Report the malaria status.
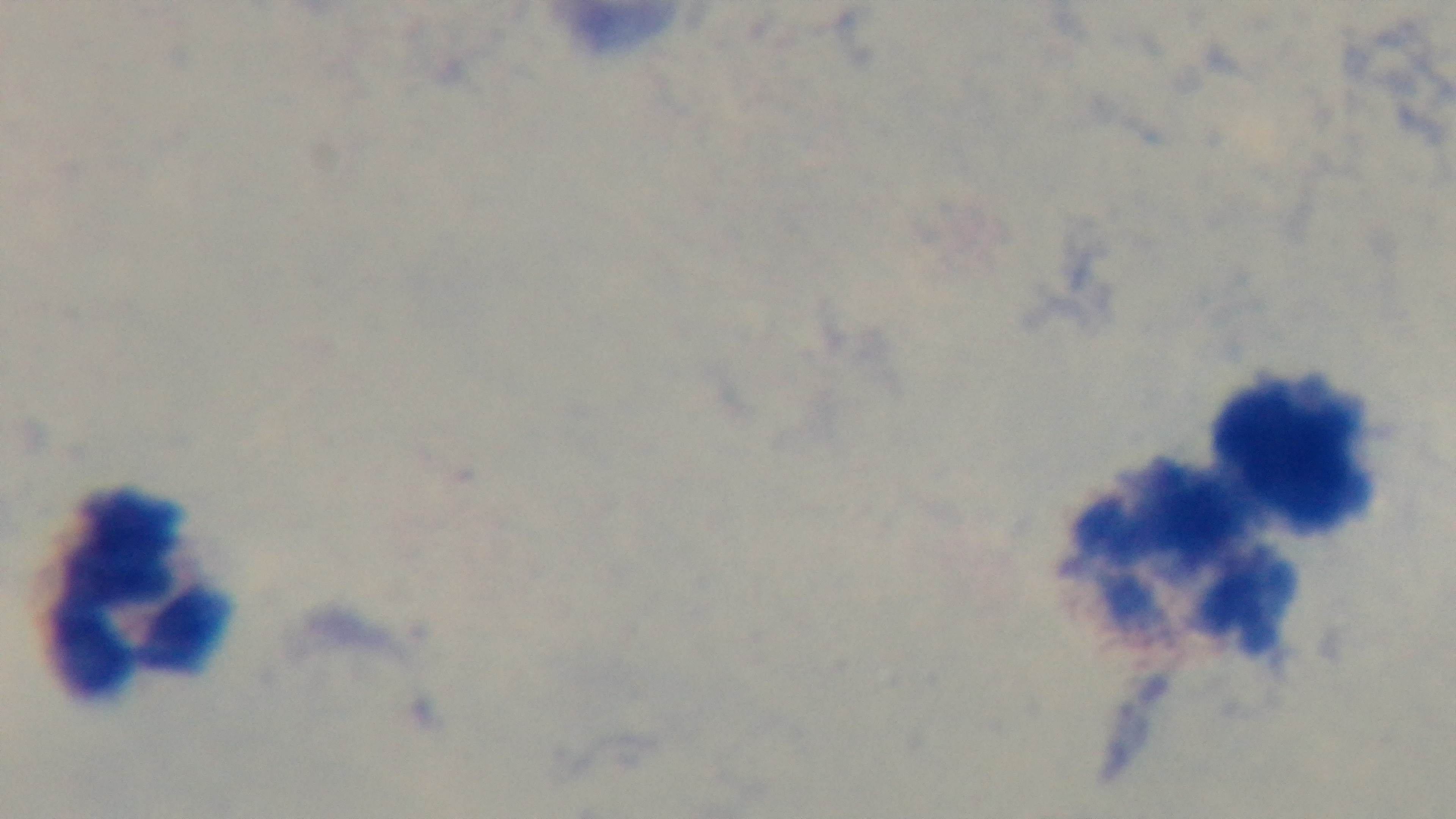
Negative.

stain = Giemsa
modality = light microscopy
preparation = thick smear
capture = mounted 4K digital camera
field of view = one from the slide
objective = 100x oil immersion